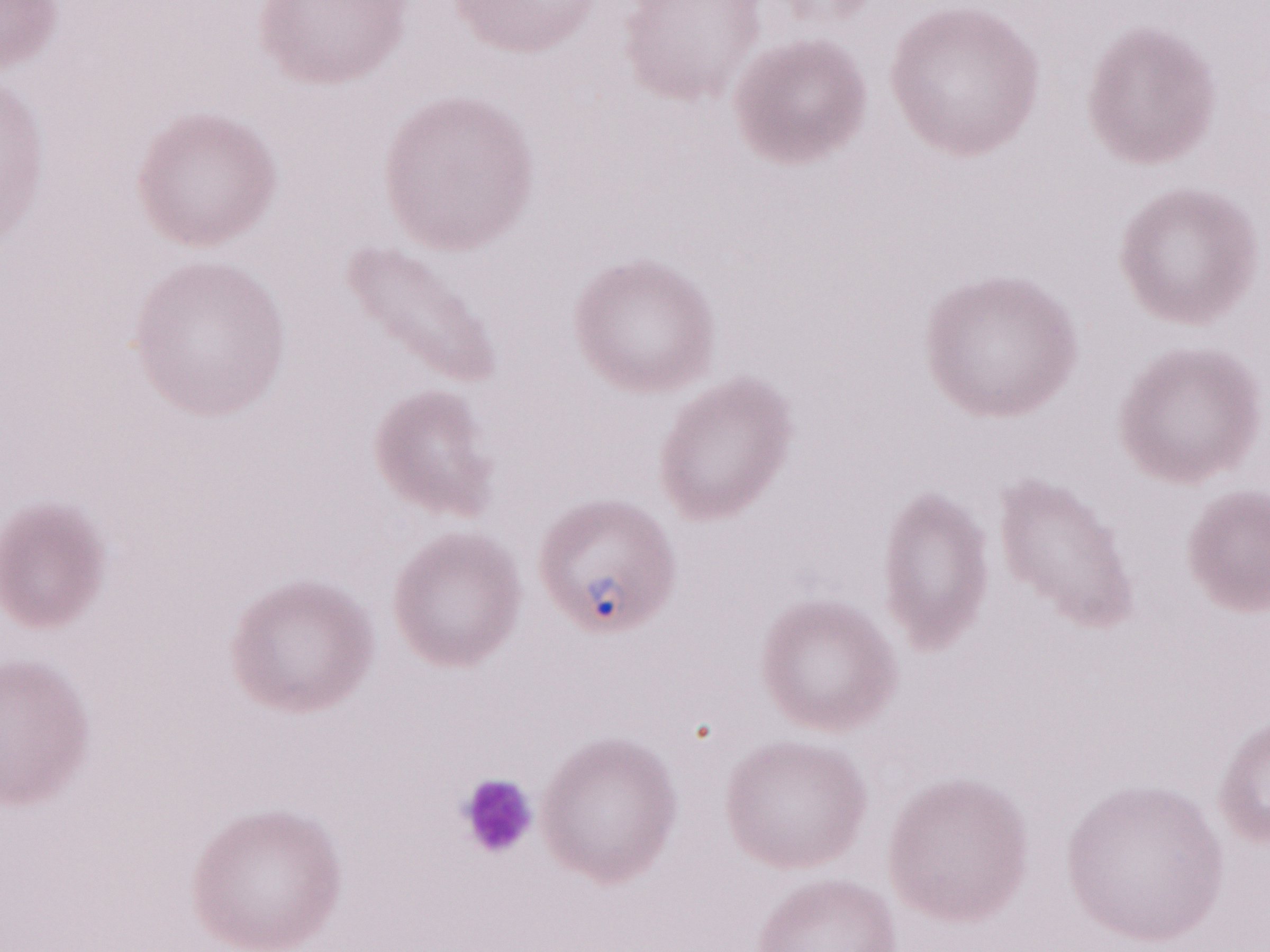 Patient diagnosis: malaria infection. Magnification: 1,000x. Olympus BX43 microscope and DP73 digital camera. Thin blood smear. May-Grünwald-Giemsa (MGG) stain. Image is 1270×952 pixels. Single field of view.